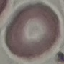
Summary:
  - Malaria status: uninfected
  - Preparation: thin smear
  - Stain: Giemsa
  - Capture: smartphone through the microscope eyepiece
  - Image type: cell patch, automatically extracted from a larger field of view and resized to 64 × 64 pixels